Classify this cell by malaria status.
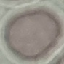

Uninfected.

Summary:
  - Image type: automatically extracted cell patch, resized to 64 × 64 pixels
  - Preparation: thin smear
  - Capture: smartphone through the microscope eyepiece
  - Stain: Giemsa